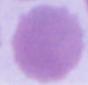
Photomicrograph. A red blood cell is shown. 1000x magnification.